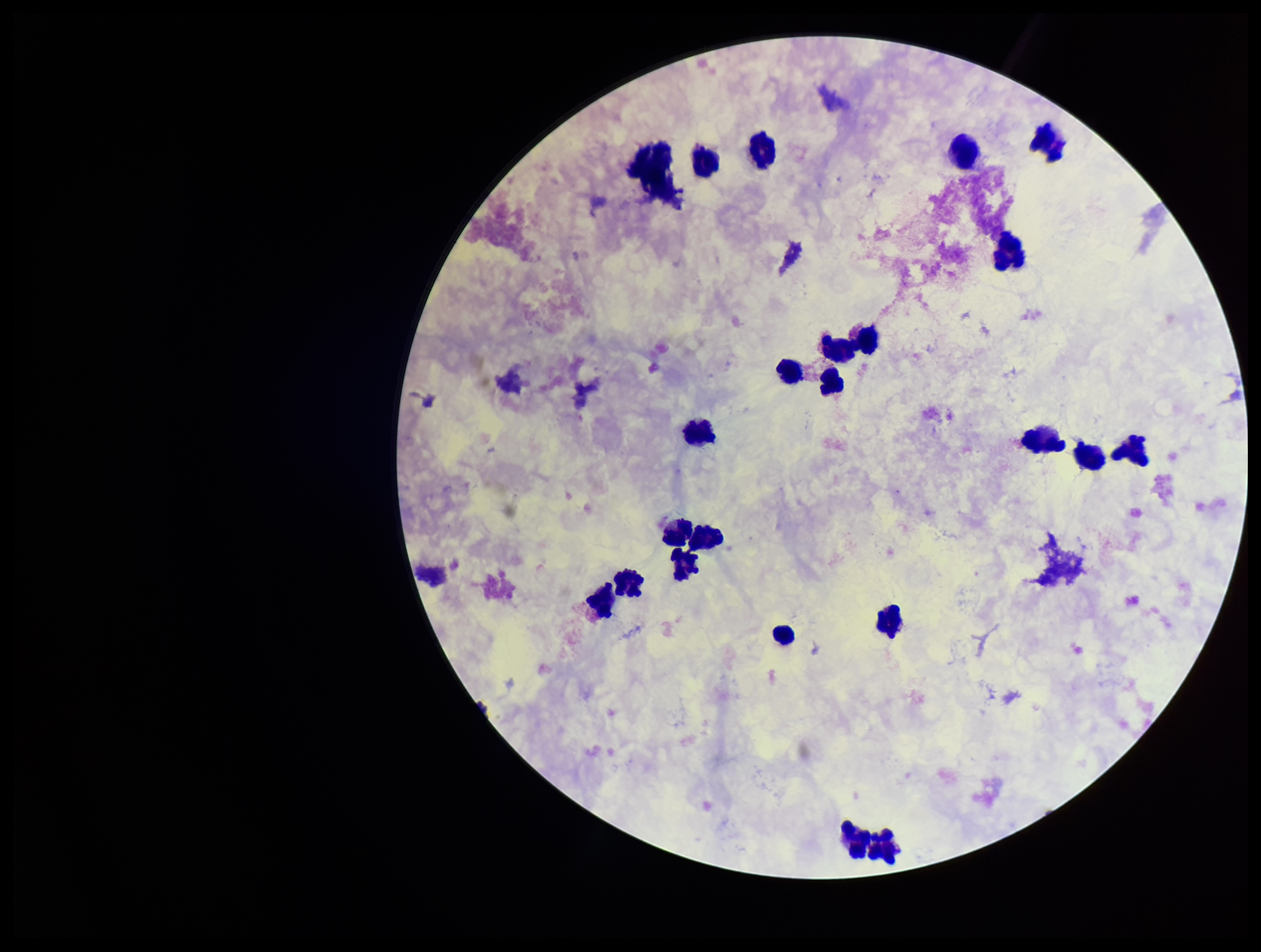 Single field of view. Parasite count: 0. Patient malaria status: negative. Giemsa stain. Image is 1261×952 pixels. Preparation: thick smear. Leukocyte count: 20. Photographed through the microscope eyepiece with a smartphone camera. Plasmodium parasites: none detected.